Name the blood parasite species.
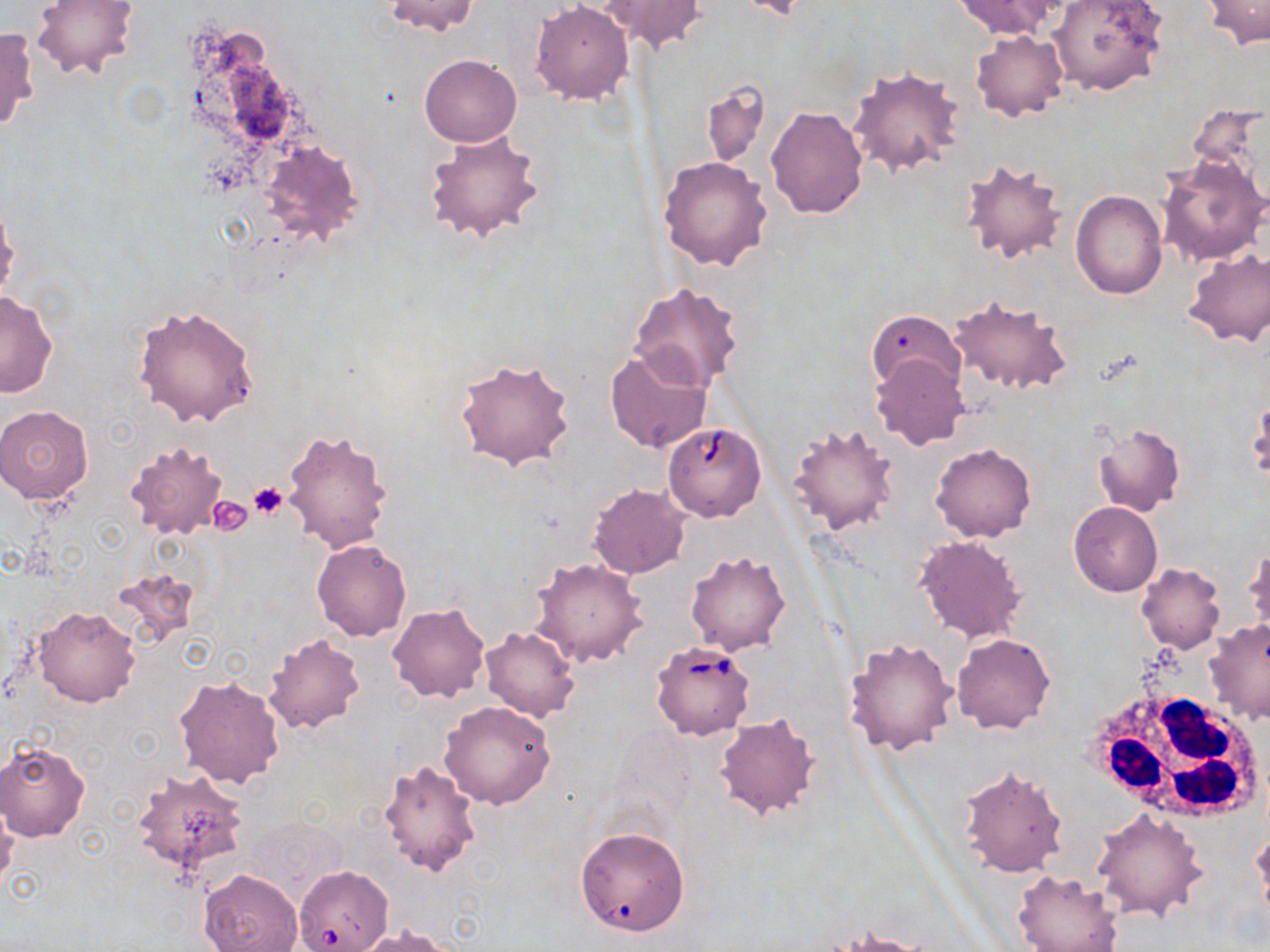

Babesia divergens.

Approximate bounding boxes as [x1, y1, x2, y2] in pixels. Babesia divergens-infected red blood cell locations: [650, 641, 756, 741], [294, 862, 389, 952]. Uninfected red blood cell locations: [31, 0, 139, 81], [380, 0, 481, 37], [951, 0, 1064, 38], [1047, 0, 1167, 97], [1201, 0, 1270, 48], [596, 1, 711, 53], [529, 2, 633, 104], [0, 26, 38, 134], [971, 30, 1067, 122], [420, 54, 521, 147], [847, 66, 967, 177], [700, 80, 770, 168], [1187, 99, 1270, 203], [766, 105, 868, 219], [422, 127, 546, 244], [256, 140, 366, 249], [659, 155, 773, 272], [1156, 156, 1268, 266], [958, 157, 1068, 267], [1070, 190, 1167, 299], [0, 202, 20, 304], [1182, 250, 1270, 348], [629, 281, 745, 390], [1, 291, 58, 397], [944, 293, 1074, 395], [131, 305, 261, 428], [867, 311, 964, 391], [611, 351, 722, 461], [869, 355, 968, 450], [451, 356, 577, 471], [1247, 398, 1269, 486], [0, 404, 97, 504], [787, 420, 899, 537], [1092, 423, 1185, 516], [666, 427, 768, 527], [280, 428, 395, 555], [123, 439, 230, 539], [930, 442, 1037, 542], [588, 484, 689, 579], [1068, 501, 1162, 597], [913, 535, 1027, 643], [311, 540, 411, 641], [1245, 543, 1269, 638], [684, 550, 793, 655], [529, 555, 649, 668], [1136, 563, 1226, 653], [388, 603, 490, 703], [33, 605, 141, 707], [1201, 620, 1270, 727], [480, 625, 579, 722], [262, 633, 365, 735], [952, 633, 1056, 734], [843, 636, 958, 756], [173, 673, 286, 789], [438, 701, 558, 808], [713, 713, 824, 822], [0, 743, 91, 842], [378, 758, 483, 877], [956, 763, 1067, 877], [132, 767, 249, 876], [0, 797, 19, 893], [1092, 808, 1208, 921], [575, 825, 691, 938], [198, 869, 301, 952], [1011, 869, 1125, 952], [352, 926, 457, 952], [833, 928, 936, 952]. Platelet locations: [247, 483, 289, 518], [209, 493, 255, 534]. White blood cell locations: [1089, 688, 1263, 823]. Captured at 1000x magnification. Image is 1270×952 pixels. Light microscopy. Thin blood smear. Single field of view. May-Grünwald-Giemsa stain.